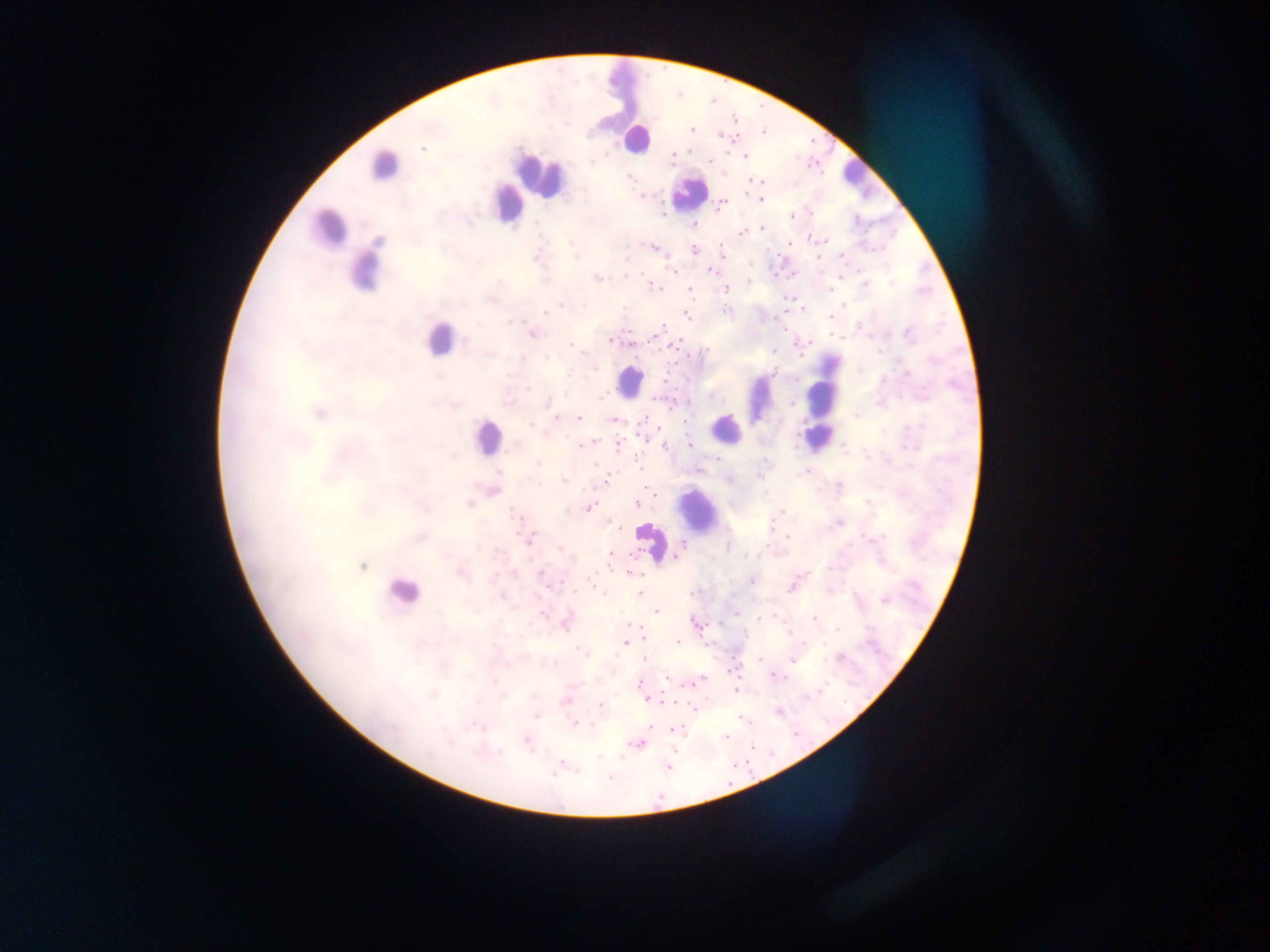

Approximate centers as x y in pixels.
Summary:
  - Leukocyte locations: 620 84; 635 138; 384 166; 540 174; 855 175; 688 193; 505 204; 328 229; 366 267; 439 339; 629 382; 759 398; 821 400; 725 428; 488 436; 816 441; 699 511; 651 542; 401 593
  - Malaria parasite locations: 692 128; 764 132; 724 136; 422 148; 745 156; 672 158; 709 162; 630 176; 755 180; 761 200; 721 203; 791 216; 694 224; 761 228; 742 233; 721 243; 790 243; 654 247; 694 250; 841 256; 575 257; 673 271; 710 271; 626 276; 597 278; 749 282; 864 285; 654 286; 689 289; 726 289; 831 289; 560 305; 727 310; 545 312; 686 315; 830 316; 859 326; 657 332; 532 334; 909 336; 610 341; 570 344; 674 345; 773 351; 879 351; 705 352; 522 358; 546 358; 593 368; 775 373; 907 373; 883 380; 663 382; 528 389; 711 395; 601 397; 548 402; 792 404; 856 415; 555 418; 578 418; 613 419; 531 426; 592 442; 581 445; 690 445; 618 446; 664 446; 844 448; 717 459; 538 463; 699 470; 804 472; 563 480; 605 481; 839 486; 637 503; 470 504; 589 508; 782 512; 516 516; 839 523; 613 524; 788 537; 530 538; 680 549; 611 554; 677 556; 746 557; 361 566; 542 572; 631 572; 752 581; 592 585; 791 587; 640 593; 884 601; 656 611; 736 613; 541 614; 760 617; 814 618; 628 624; 696 624; 836 629; 789 633; 677 641; 625 644; 579 650; 644 658; 760 659; 792 659; 731 671; 776 676; 666 678; 495 681; 697 681; 640 683; 693 683; 735 690; 648 699; 566 701; 601 707; 537 715; 742 718; 576 722; 650 727; 676 729; 726 736; 527 740; 635 743; 752 748; 563 764; 668 767; 610 777
  - Image size: 1270×952 pixels
  - Preparation: thick blood smear
  - Country: Ghana
  - Capture: mobile-phone photograph through a microscope
  - Field of view: single